Classify this cell by malaria status.
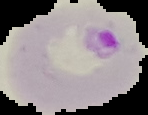

Parasitized.

Summary:
  - Image type: segmented cell region with the area outside set to black
  - Preparation: thin blood film
  - Image size: 148×115 pixels